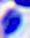
identification = leukocyte
magnification = 400x
modality = photomicrograph